State the preparation type.
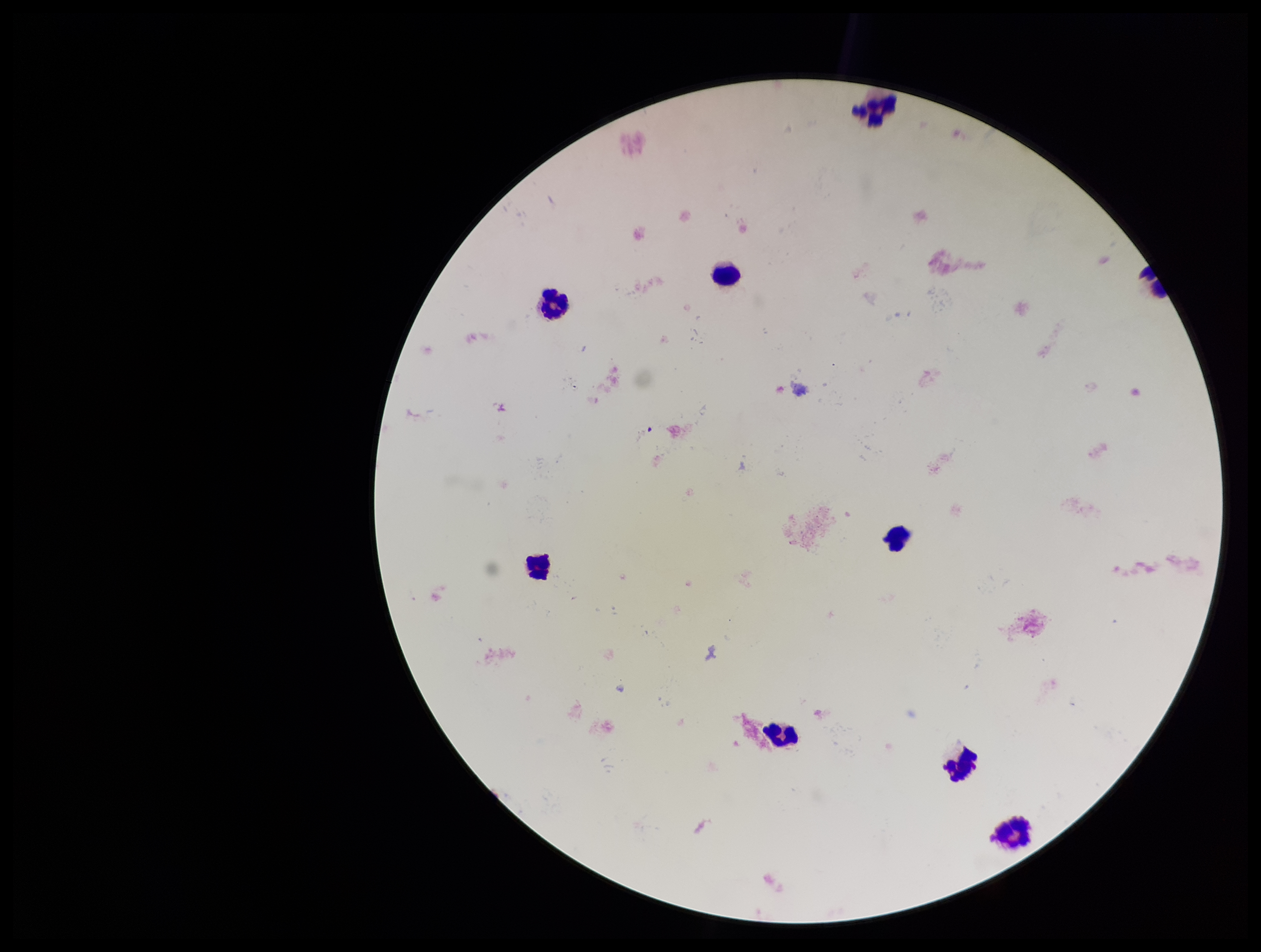
Thick.

Leukocyte count: 8. Smartphone photograph taken through the eyepiece of a microscope. Patient malaria status: negative. Image is 1261×952 pixels. One field from this slide. Parasite count: 0. Plasmodium parasites: none detected. Giemsa stain.